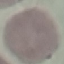

Summary:
  - Result: negative for malaria parasites
  - Stain: Giemsa
  - Capture: smartphone through the microscope eyepiece
  - Preparation: thin blood smear
  - Image type: cell patch, automatically extracted from a larger field of view and resized to 64 × 64 pixels